Report the malaria status of this cell.
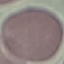

It is uninfected.

Summary:
  - Capture: smartphone through the microscope eyepiece
  - Preparation: thin smear
  - Stain: Giemsa
  - Image type: automatically extracted cell patch, resized to 64 × 64 pixels